Assess this cell for malaria.
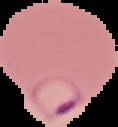

It is parasitized.

preparation = thin blood smear
image type = segmented cell region on a black background
image size = 118×127 pixels